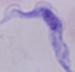
modality: photomicrograph
magnification: 1000x
identification: trypanosome